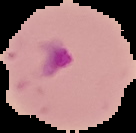

Summary:
  - Image size: 136×133 pixels
  - Preparation: thin blood smear
  - Result: malaria parasites identified
  - Image type: segmented cell region on a black background